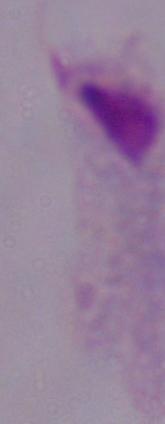
A trichomonad is seen. Photomicrograph. Captured at 1000x magnification.